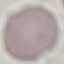

Malaria status: uninfected. Giemsa-stained preparation. Photographed with a smartphone camera at the microscope eyepiece. Cell patch, automatically extracted from a larger field of view and resized to 64 × 64 pixels. Thin blood smear.